Name the blood parasite species.
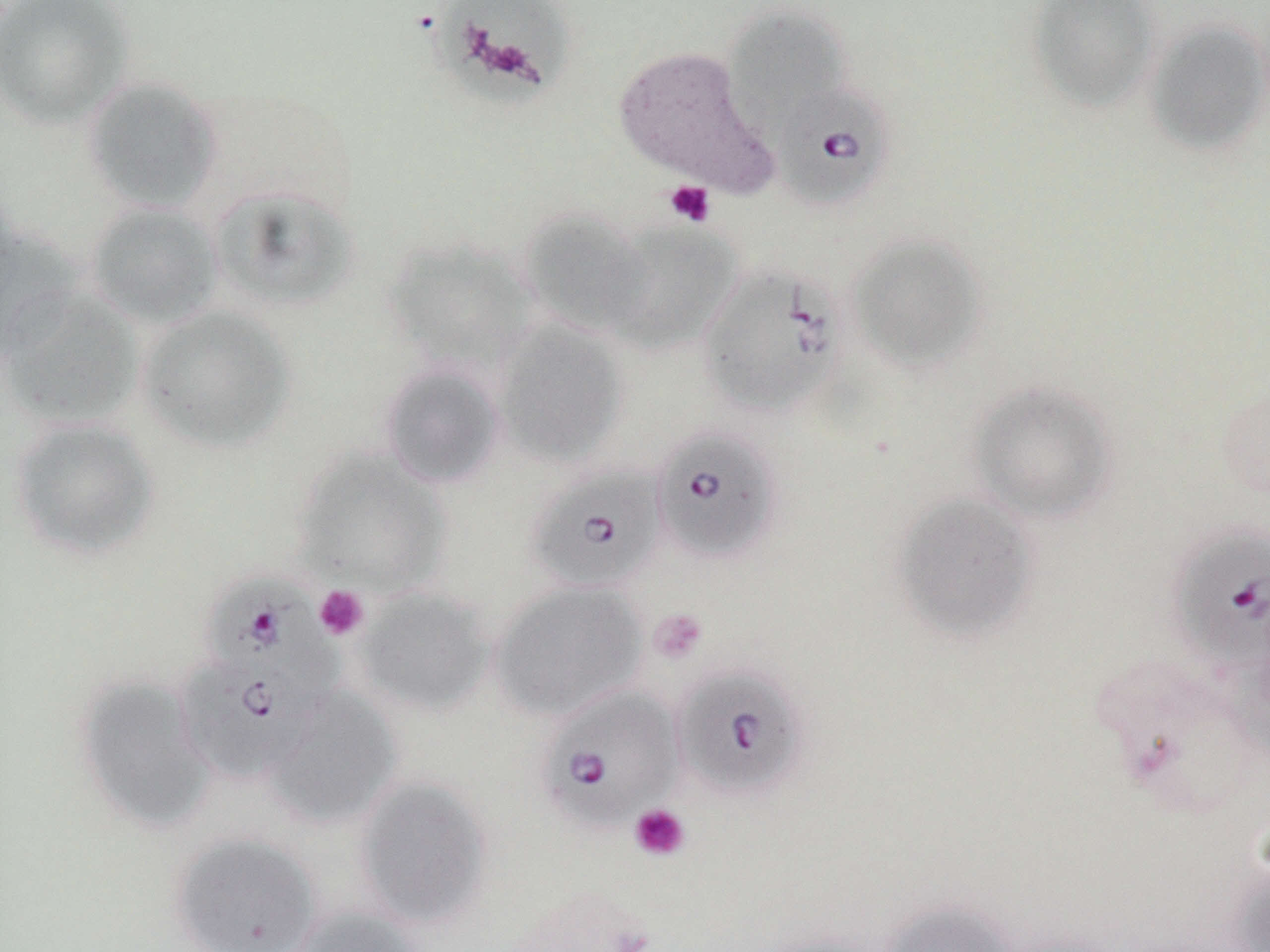

Babesia divergens.

field of view = single
uninfected red blood cell locations = approximate bounding boxes as [x1, y1, x2, y2] in pixels: [0, 0, 135, 128], [435, 0, 575, 97], [1028, 0, 1161, 110], [723, 6, 849, 127], [1145, 20, 1270, 155], [612, 45, 775, 195], [81, 76, 223, 215], [209, 185, 359, 313], [85, 202, 224, 329], [518, 207, 654, 337], [603, 223, 742, 354], [0, 228, 84, 361], [845, 232, 988, 372], [383, 238, 538, 376], [2, 290, 143, 428], [137, 304, 297, 453], [492, 320, 630, 468], [379, 362, 506, 489], [966, 380, 1120, 525], [8, 418, 160, 561], [291, 447, 451, 596], [891, 492, 1041, 641], [490, 580, 647, 722], [355, 588, 494, 716], [74, 675, 215, 832], [265, 687, 402, 828], [354, 774, 493, 929], [169, 831, 322, 952], [1228, 861, 1270, 952], [879, 900, 1022, 952], [292, 905, 424, 952], [1001, 928, 1134, 952]
platelet locations = approximate bounding boxes as [x1, y1, x2, y2] in pixels: [664, 180, 716, 227], [314, 585, 370, 640], [649, 608, 708, 664], [629, 803, 691, 862]
magnification = 1000x
image size = 1270×952 pixels
Babesia divergens-infected red blood cell locations = approximate bounding boxes as [x1, y1, x2, y2] in pixels: [773, 82, 895, 210], [697, 262, 847, 418], [651, 426, 783, 565], [526, 464, 666, 593], [1167, 525, 1270, 672], [202, 569, 344, 708], [176, 657, 318, 782], [673, 663, 810, 800], [536, 685, 684, 835]
modality = light microscopy
preparation = thin blood film
stain = May-Grünwald-Giemsa